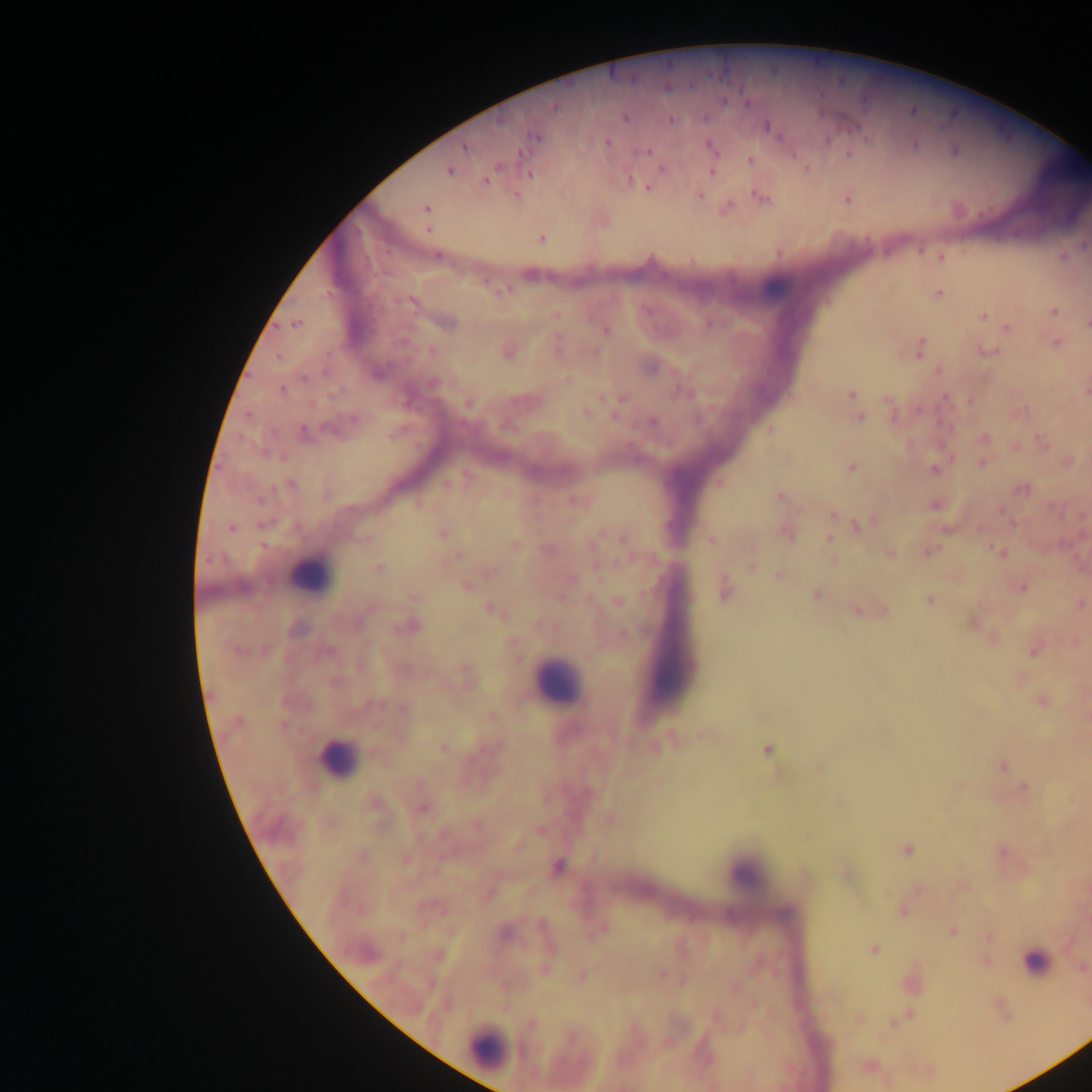
image size = 1092×1092 pixels
country = Ghana
preparation = thick blood smear
leukocyte locations = approximate centers as [x, y] in pixels: [308, 576], [556, 683], [337, 759], [743, 873], [1035, 962], [488, 1049]
field of view = single
malaria parasite locations = approximate centers as [x, y] in pixels: [553, 107], [913, 111], [625, 116], [670, 119], [767, 126], [535, 136], [607, 142], [915, 144], [464, 145], [708, 145], [955, 150], [648, 151], [750, 159], [661, 168], [806, 168], [448, 170], [711, 170], [528, 173], [486, 180], [630, 180], [637, 183], [647, 186], [516, 195], [698, 195], [761, 197], [846, 198], [725, 207], [427, 209], [540, 238], [1082, 244], [436, 255], [1062, 256], [940, 257], [500, 291], [937, 292], [410, 302], [1053, 310], [555, 315], [982, 316], [446, 322], [1086, 323], [296, 324], [1006, 327], [605, 330], [1055, 342], [555, 346], [920, 348], [506, 350], [986, 351], [567, 380], [282, 388], [1085, 390], [851, 394], [621, 400], [971, 401], [468, 404], [892, 410], [1018, 410], [585, 411], [858, 417], [652, 421], [337, 425], [769, 429], [302, 432], [983, 438], [1043, 442], [1014, 446], [982, 462], [1068, 462], [850, 467], [934, 468], [446, 482], [718, 483], [290, 484], [1021, 489], [780, 496], [575, 500], [935, 504], [832, 514], [1011, 520], [859, 524], [831, 527], [231, 528], [786, 532], [442, 533], [830, 537], [364, 538], [623, 539], [711, 540], [513, 544], [928, 551], [1000, 552], [888, 554], [458, 555], [751, 566], [379, 567], [489, 571], [778, 575], [466, 584], [1020, 587], [723, 590], [815, 595], [413, 596], [929, 600], [617, 601], [1080, 603], [490, 607], [859, 609], [878, 610], [972, 622], [408, 625], [622, 633], [994, 638], [1075, 642], [1034, 648], [464, 675], [1042, 701], [403, 708], [491, 716], [701, 733], [656, 746], [442, 747], [767, 749], [1002, 765], [819, 766], [1024, 788], [421, 808], [609, 818], [539, 829], [517, 846], [907, 849], [1001, 852], [361, 856], [405, 860], [558, 865], [845, 875], [959, 884], [916, 890], [489, 891], [903, 910], [601, 927], [951, 930], [503, 931], [989, 937], [873, 949], [985, 961], [1081, 967], [544, 970], [659, 974], [580, 977], [681, 980], [1001, 1007], [908, 1014], [715, 1015], [859, 1017], [530, 1024], [868, 1065]
capture = mobile-phone photograph through a microscope